Comment on the morphology of the red blood cells.
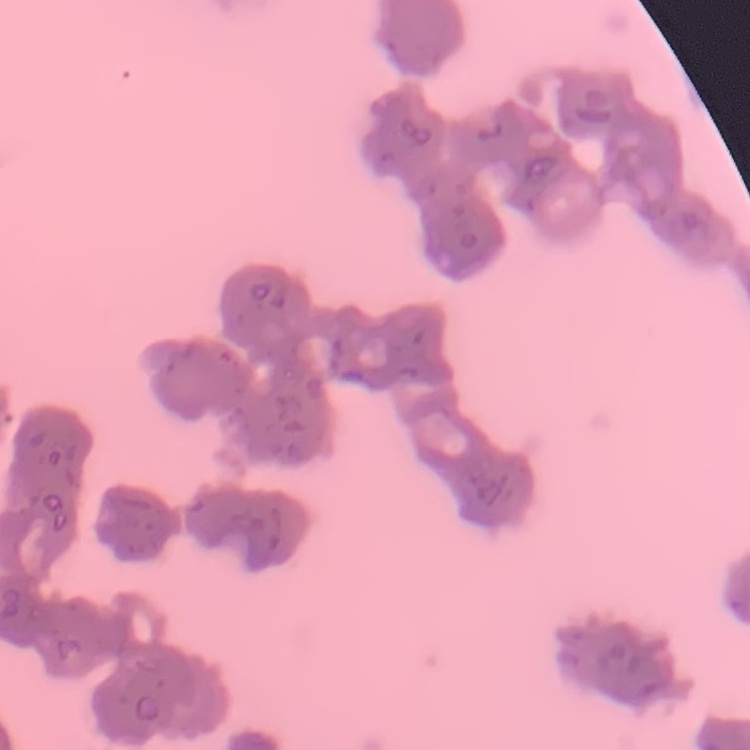
Rouleaux formation.

Summary:
  - Preparation: thin peripheral smear
  - Stain: Field's or Giemsa
  - Image type: square crop of a larger photomicrograph